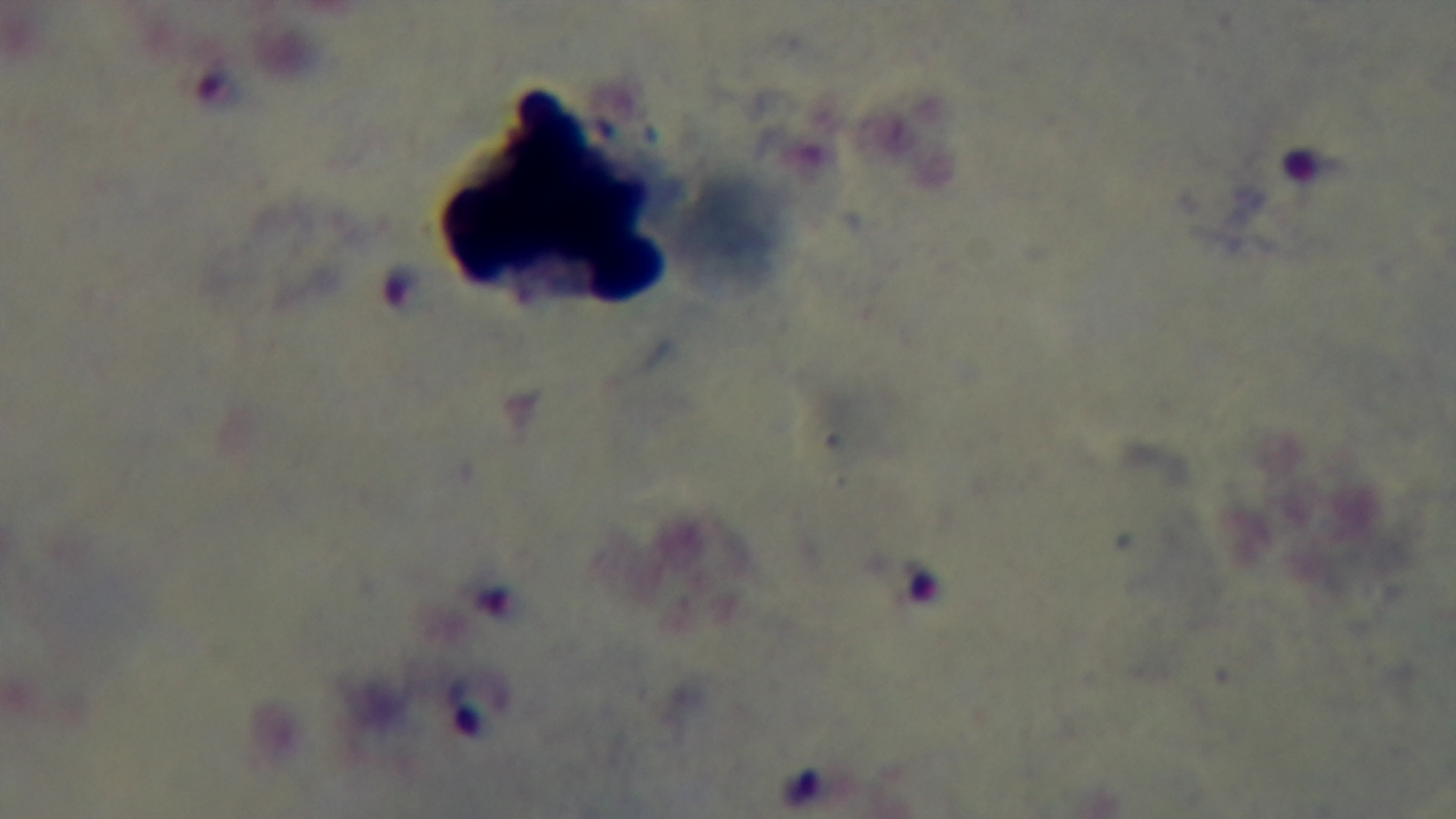

Oil-immersion objective, 100x. Malaria status: positive. One field from the slide. Giemsa-stained. Preparation: thick smear. Light microscopy. Mounted 4K digital camera.